Comment on the morphology of the red blood cells.
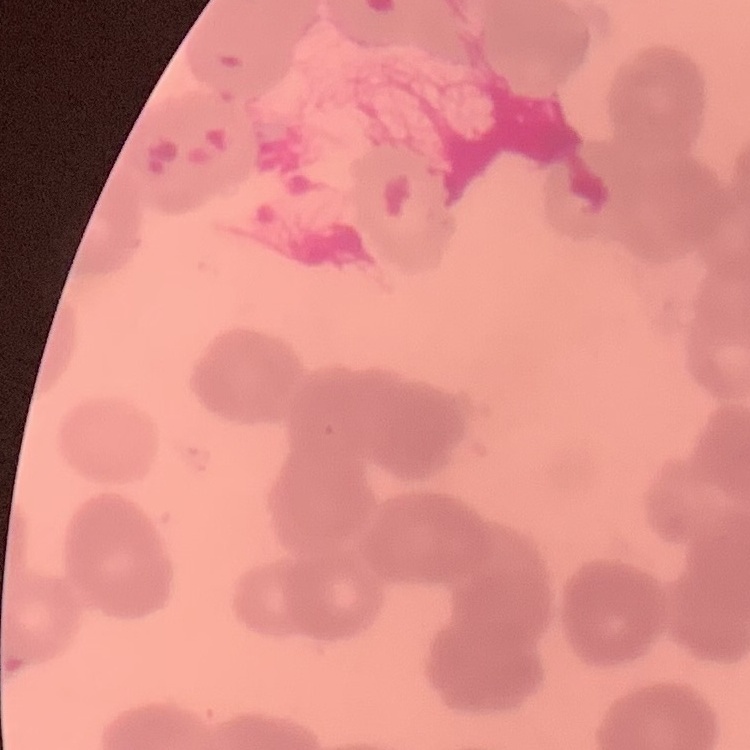
Rouleaux formation.

Thin blood film. Square crop of a larger photomicrograph. Stained with either Field's or Giemsa.